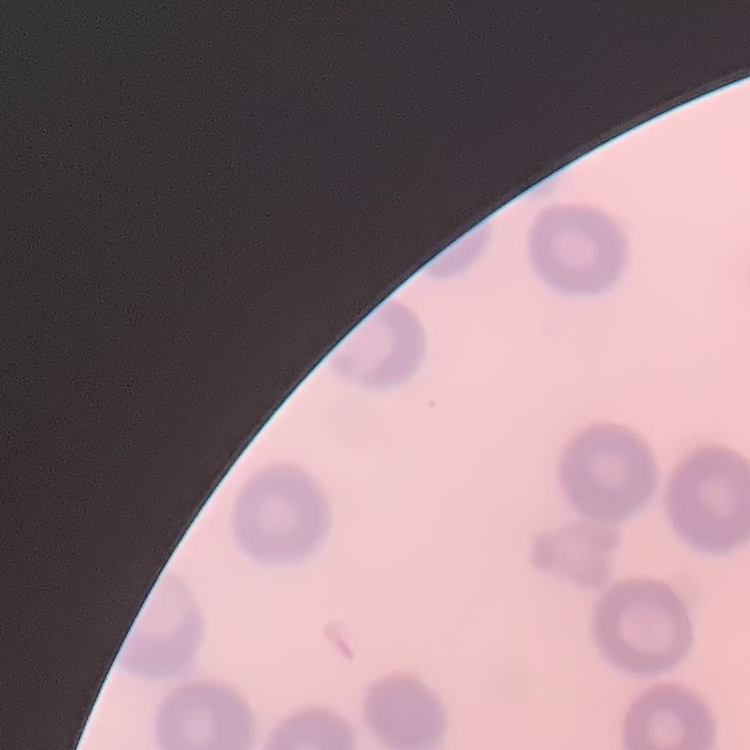

red_blood_cell_morphology: no rouleaux formation
image_type: square crop of a larger photomicrograph
preparation: thin peripheral smear
stain: Field's or Giemsa